Evaluate for malaria.
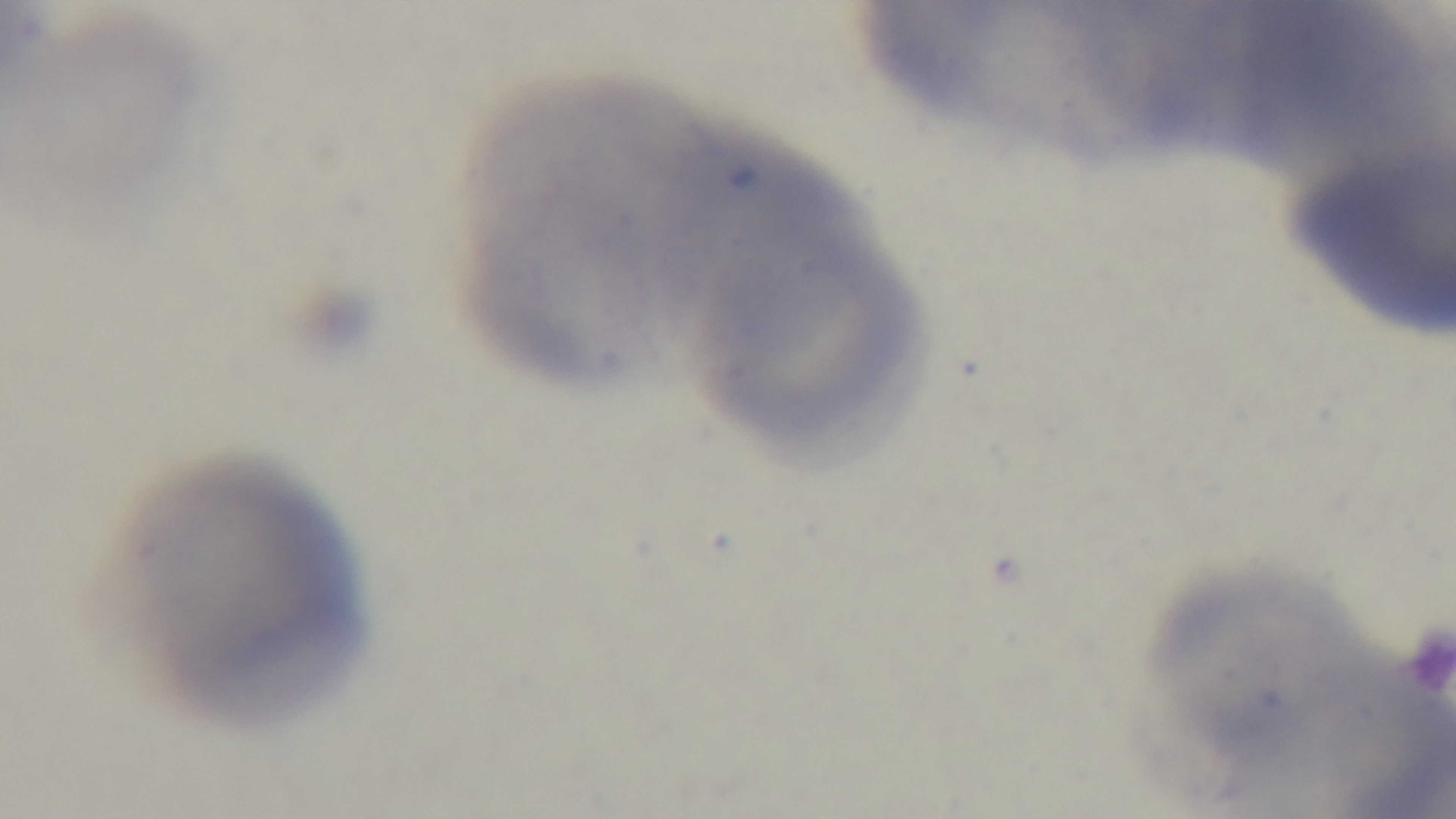

It is uninfected.

Giemsa-stained. Preparation: thin. Single field of view. Photomicrograph. 100x oil-immersion objective. Mounted 4K digital camera.